Assess the morphology of the red blood cells.
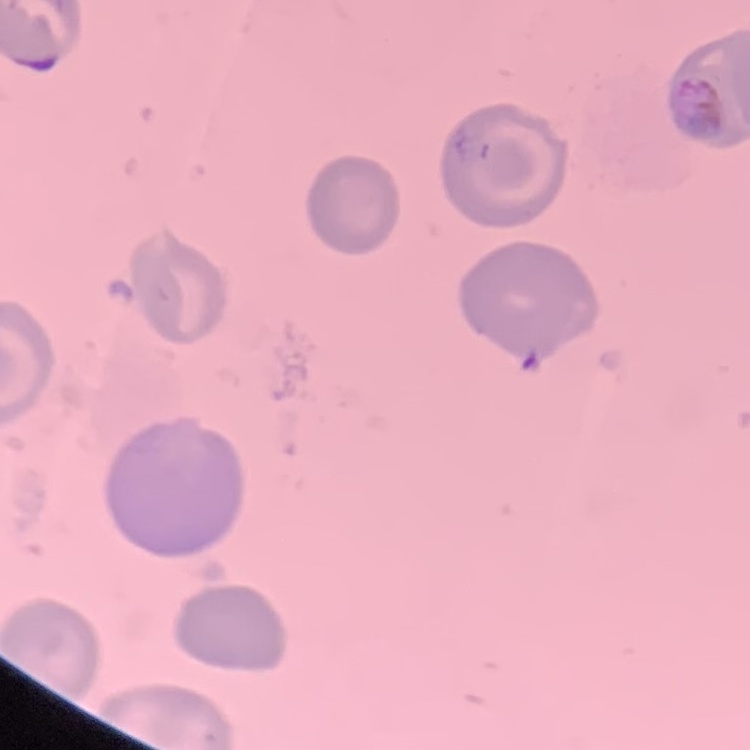

They show no rouleaux formation.

{
  "image_type": "one tile cut from a larger photomicrograph",
  "preparation": "thin blood film",
  "stain": "Field's or Giemsa"
}